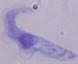
modality = micrograph
identification = trypanosome
magnification = 1000x